Report the malaria status of this cell.
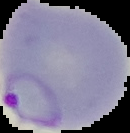
Parasitized.

{
  "image_size": "130×133 pixels",
  "image_type": "segmented cell region with the area outside set to black",
  "preparation": "thin blood smear"
}